Look for Plasmodium parasites.
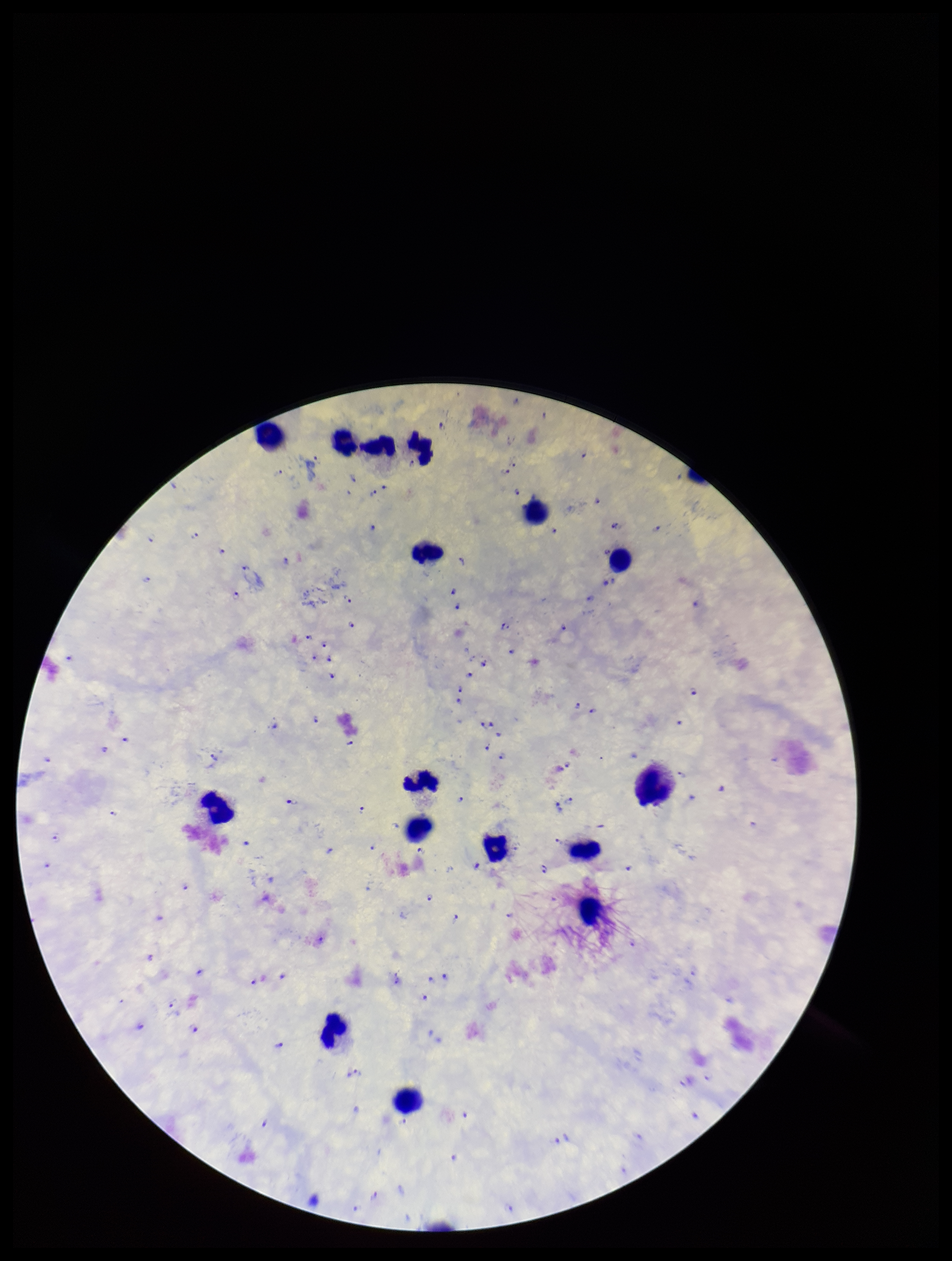
Identified.

Summary:
  - Species reported for this patient: Plasmodium falciparum
  - Preparation: thick blood smear
  - Capture: smartphone photograph through the microscope eyepiece
  - Stain: Giemsa
  - Patient malaria status: infected
  - Leukocyte count: 16
  - Image size: 952×1261 pixels
  - Parasite count: 96
  - Field of view: single